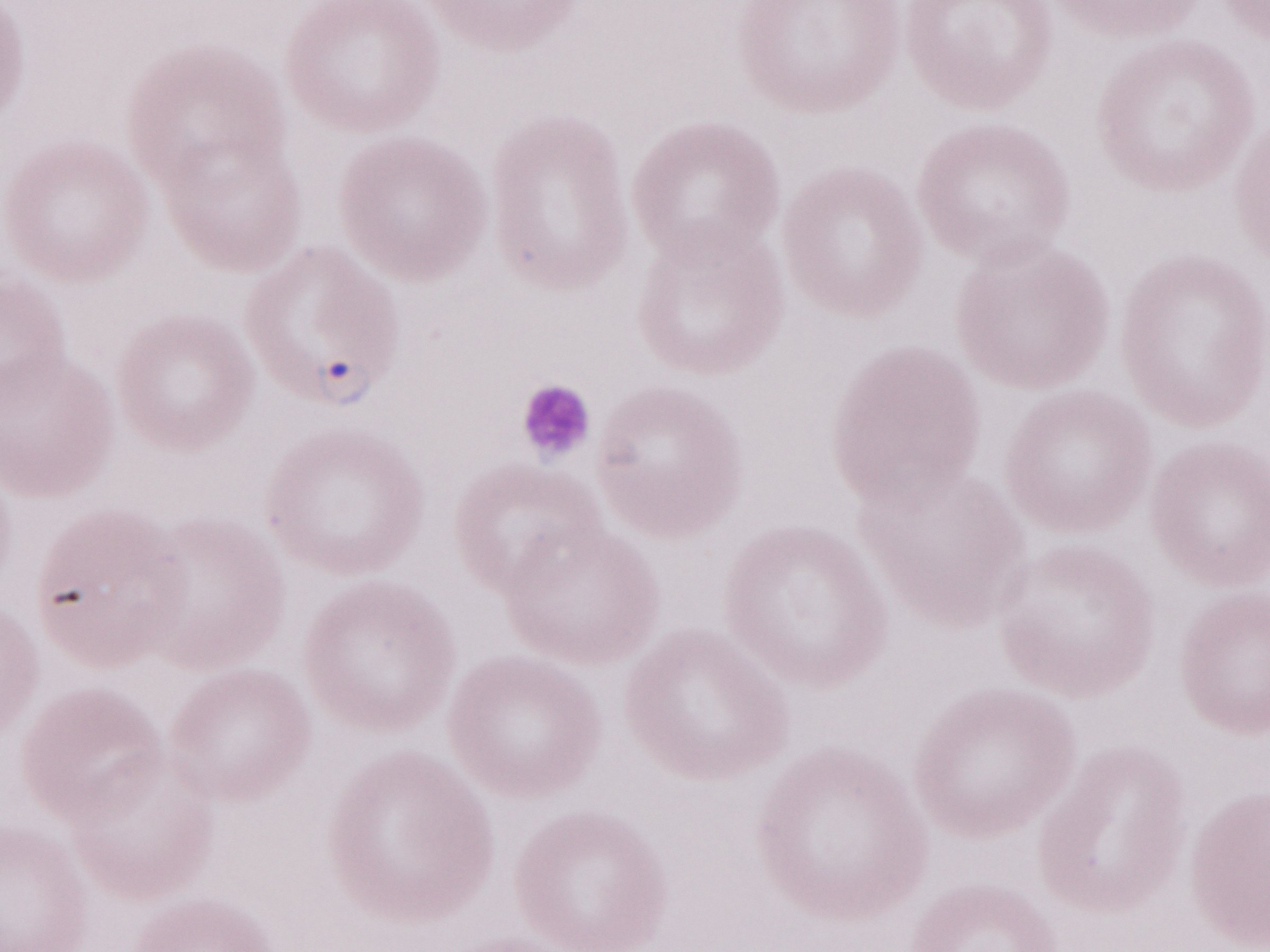

Thin blood smear. Single field of view. Olympus BX43 microscope and DP73 digital camera. Image is 1270×952 pixels. 1,000x magnification. May-Grünwald-Giemsa stain. Patient diagnosis: malaria infection.